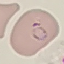

Malaria status: parasitized. Giemsa stain. Acquired by smartphone through the microscope eyepiece. Thin blood film. Automatically extracted cell patch, resized to 64 × 64 pixels.